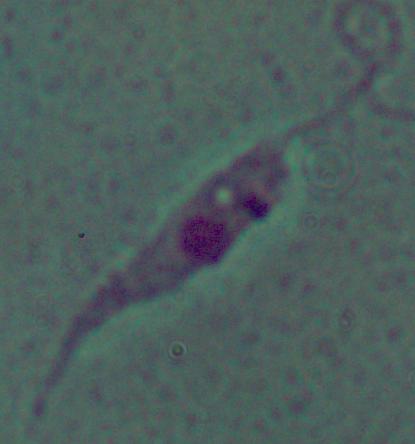
1000x magnification. A Leishmania parasite is shown. Photomicrograph.